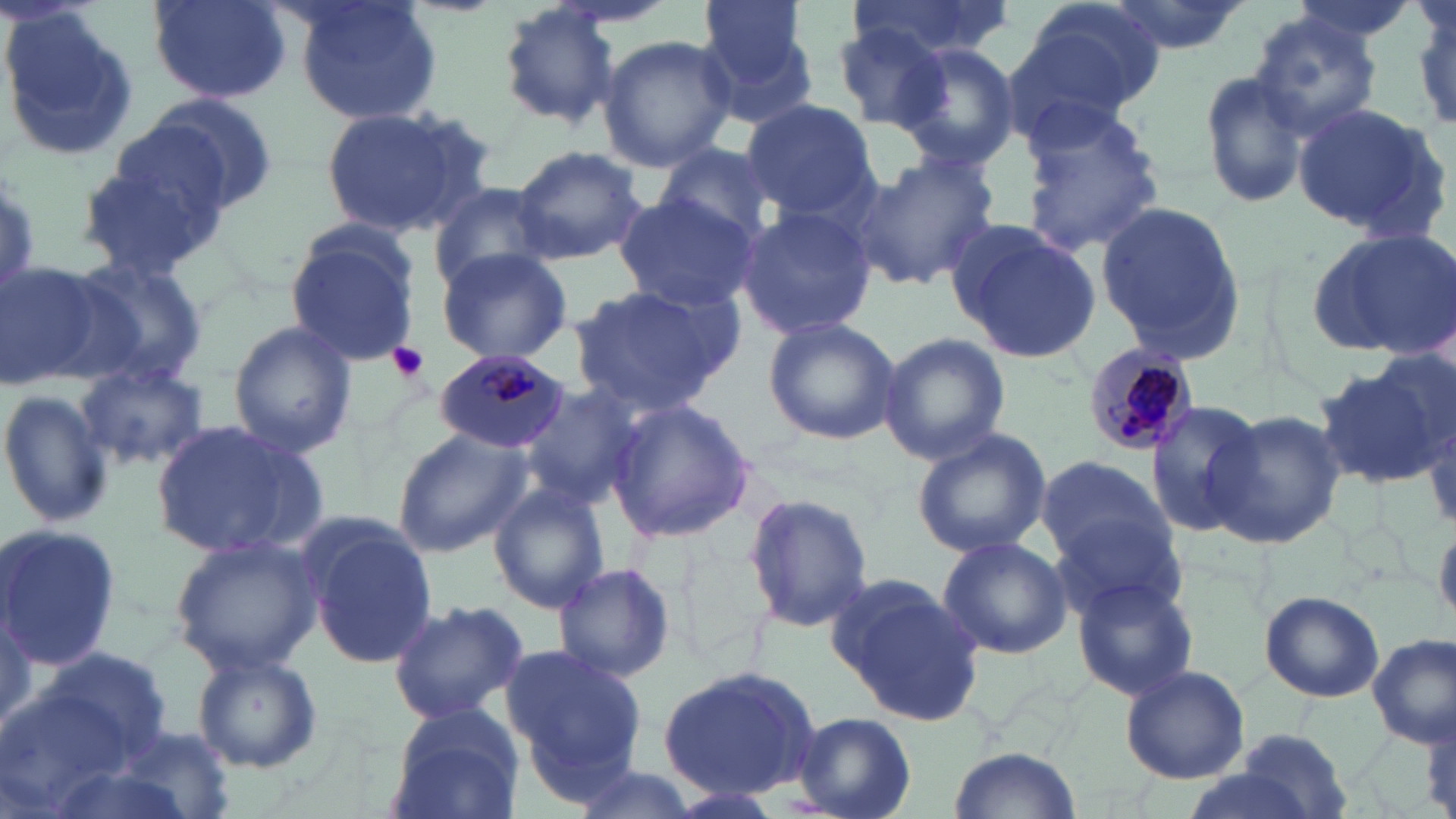
Approximate bounding boxes as named x1/y1/x2/y2 corners in pixels. Uninfected red blood cell locations: (x1=149, y1=0, x2=292, y2=105), (x1=292, y1=0, x2=443, y2=128), (x1=694, y1=0, x2=817, y2=125), (x1=850, y1=0, x2=1017, y2=60), (x1=1016, y1=0, x2=1166, y2=117), (x1=1104, y1=0, x2=1250, y2=55), (x1=1409, y1=0, x2=1456, y2=134), (x1=496, y1=4, x2=623, y2=131), (x1=0, y1=10, x2=142, y2=161), (x1=1248, y1=11, x2=1386, y2=141), (x1=833, y1=25, x2=953, y2=131), (x1=597, y1=35, x2=736, y2=173), (x1=895, y1=42, x2=1021, y2=172), (x1=1199, y1=67, x2=1316, y2=210), (x1=140, y1=91, x2=282, y2=213), (x1=738, y1=99, x2=879, y2=221), (x1=1293, y1=103, x2=1450, y2=242), (x1=313, y1=106, x2=480, y2=236), (x1=1020, y1=109, x2=1166, y2=256), (x1=72, y1=139, x2=234, y2=281), (x1=510, y1=145, x2=647, y2=263), (x1=653, y1=146, x2=778, y2=247), (x1=853, y1=154, x2=1000, y2=289), (x1=426, y1=184, x2=560, y2=293), (x1=611, y1=191, x2=760, y2=311), (x1=1094, y1=202, x2=1245, y2=361), (x1=734, y1=206, x2=877, y2=341), (x1=947, y1=221, x2=1101, y2=362), (x1=285, y1=222, x2=423, y2=365), (x1=1304, y1=228, x2=1454, y2=358), (x1=435, y1=247, x2=576, y2=365), (x1=64, y1=253, x2=208, y2=385), (x1=0, y1=260, x2=121, y2=391), (x1=566, y1=285, x2=735, y2=417), (x1=762, y1=316, x2=900, y2=445), (x1=227, y1=319, x2=357, y2=457), (x1=878, y1=331, x2=1012, y2=465), (x1=1319, y1=358, x2=1451, y2=485), (x1=74, y1=360, x2=209, y2=471), (x1=511, y1=381, x2=645, y2=508), (x1=0, y1=386, x2=116, y2=532), (x1=608, y1=398, x2=759, y2=543), (x1=1143, y1=400, x2=1270, y2=538), (x1=1208, y1=411, x2=1348, y2=548), (x1=150, y1=417, x2=329, y2=560), (x1=392, y1=424, x2=535, y2=557), (x1=913, y1=426, x2=1052, y2=558), (x1=1035, y1=453, x2=1172, y2=571), (x1=488, y1=482, x2=612, y2=614), (x1=741, y1=491, x2=874, y2=631), (x1=1049, y1=511, x2=1190, y2=622), (x1=300, y1=516, x2=438, y2=671), (x1=1, y1=523, x2=120, y2=673), (x1=168, y1=534, x2=325, y2=676), (x1=936, y1=535, x2=1072, y2=660), (x1=550, y1=561, x2=677, y2=685), (x1=1071, y1=575, x2=1201, y2=701), (x1=829, y1=577, x2=984, y2=728), (x1=1258, y1=590, x2=1384, y2=703), (x1=386, y1=599, x2=529, y2=723), (x1=1300, y1=614, x2=1456, y2=736), (x1=1369, y1=633, x2=1453, y2=748), (x1=32, y1=642, x2=175, y2=771), (x1=500, y1=644, x2=648, y2=781), (x1=189, y1=649, x2=323, y2=775), (x1=657, y1=663, x2=823, y2=801), (x1=1120, y1=666, x2=1251, y2=784), (x1=0, y1=681, x2=151, y2=816), (x1=385, y1=705, x2=522, y2=819), (x1=794, y1=712, x2=916, y2=819), (x1=113, y1=726, x2=238, y2=818), (x1=1229, y1=729, x2=1355, y2=816), (x1=947, y1=746, x2=1083, y2=819), (x1=560, y1=761, x2=702, y2=819), (x1=1176, y1=767, x2=1327, y2=819), (x1=653, y1=783, x2=787, y2=819). Platelet locations: (x1=387, y1=342, x2=429, y2=383). Plasmodium malariae-infected red blood cell locations: (x1=1081, y1=343, x2=1203, y2=455), (x1=435, y1=348, x2=571, y2=454). Slide-level diagnosis: Plasmodium malariae. Thin blood film. One field of a larger specimen. Light microscopy. 1000x magnification. May-Grünwald-Giemsa-stained preparation. Image is 1456×819 pixels.